Name the parasite shown.
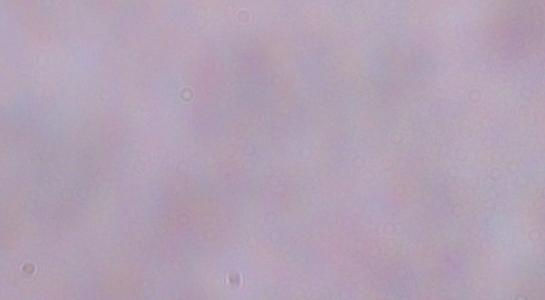

A trypanosome.

Micrograph. Captured at 1000x magnification.